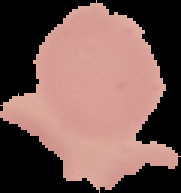

Image is 181×193 pixels. From a thin blood smear. Malaria status: uninfected. Segmented cell region on a black background.